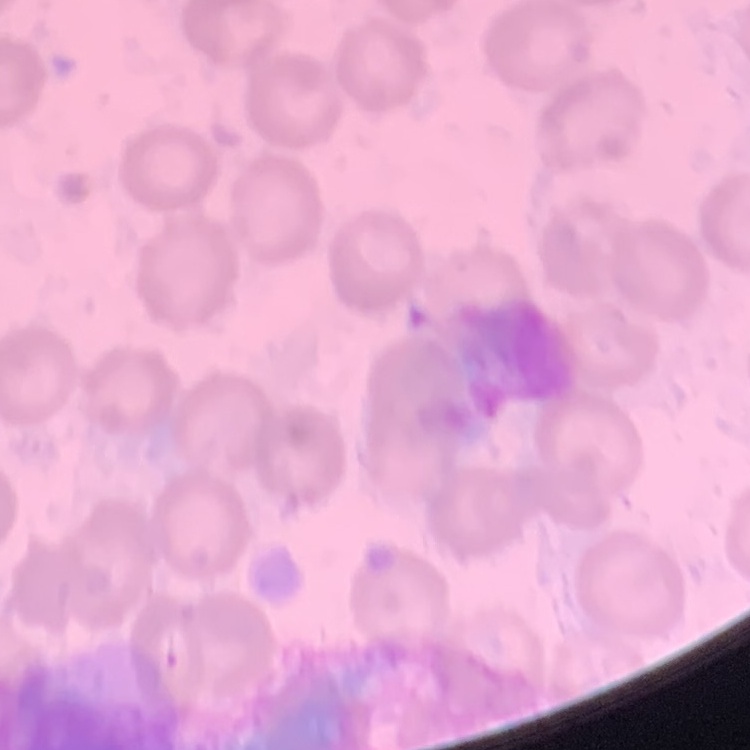 The red blood cells exhibit no rouleaux formation. Thin blood film. Square crop of a larger photomicrograph. Stained with either Field's or Giemsa.